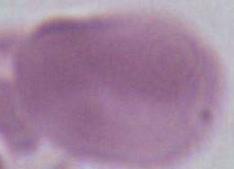 Photomicrograph. An erythrocyte is seen. Captured at 1000x magnification.